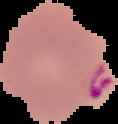
Image is 118×124 pixels. Segmented cell region on a black background. From a thin blood film. Result: malaria parasites detected.